Classify this cell by malaria status.
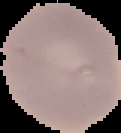

Uninfected.

image_type: segmented cell region on a black background
image_size: 121×133 pixels
preparation: thin blood film